Classify this cell by malaria status.
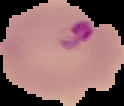

Parasitized.

Summary:
  - Image size: 124×106 pixels
  - Image type: segmented cell region on a black background
  - Preparation: thin blood film